State which parasite is depicted.
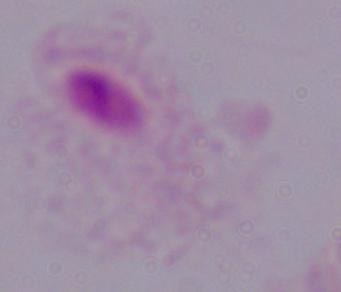

A trichomonad.

Captured at 1000x magnification. Photomicrograph.